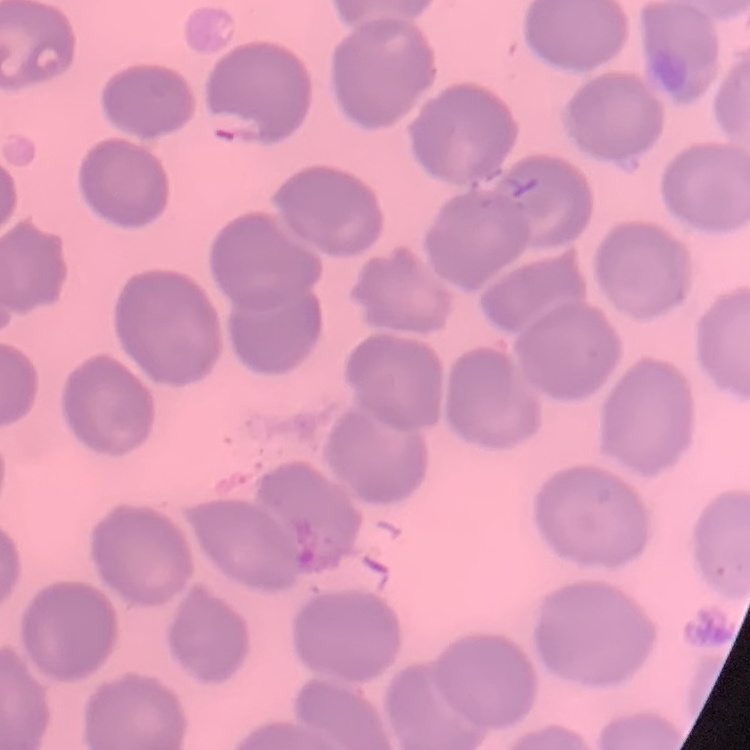
The red blood cells show no rouleaux formation. One tile cut from a larger photomicrograph. Thin blood smear. Field's or Giemsa stain.